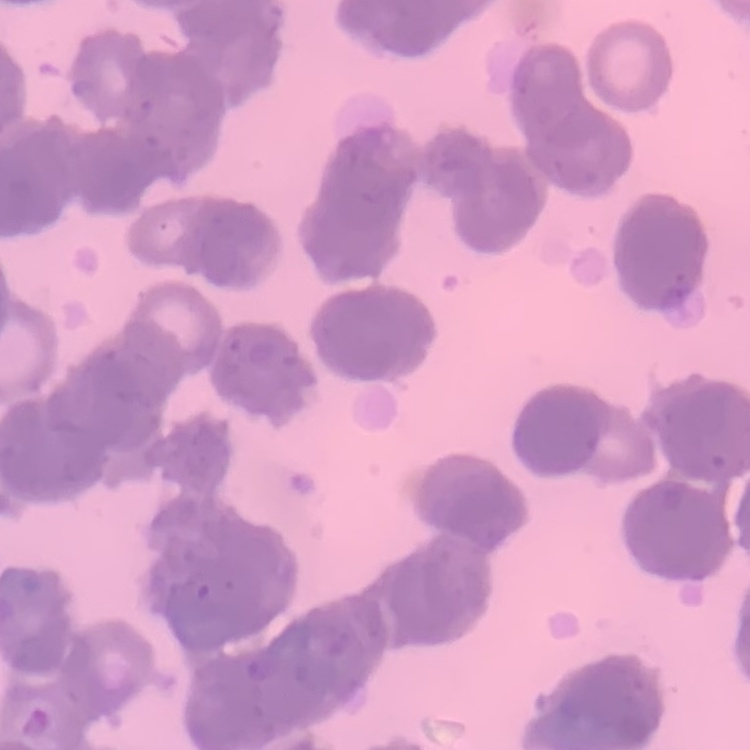 The erythrocytes show rouleaux formation. Square crop of a larger photomicrograph. Stained with either Field's or Giemsa. Thin blood film.